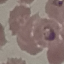

Malaria status: parasitized. Automatically extracted cell patch, resized to 64 × 64 pixels. Thin blood film. Giemsa stain. Photographed with a smartphone camera at the microscope eyepiece.